Assess the morphology of the red blood cells.
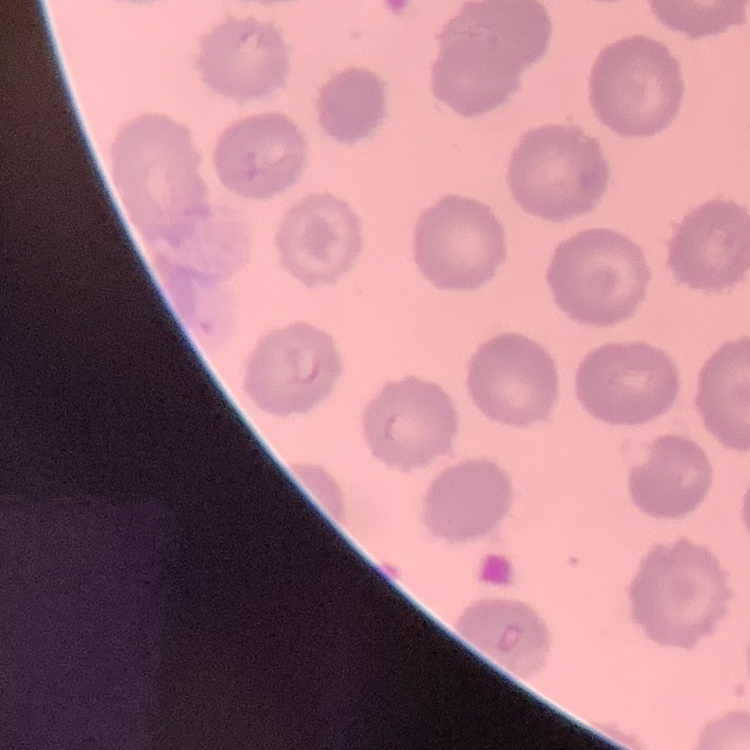

No rouleaux formation.

Field's or Giemsa stain. Thin peripheral smear. Square crop of a larger photomicrograph.